Report the malaria status of this cell.
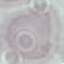

Uninfected.

capture = smartphone through the microscope eyepiece
preparation = thin smear
stain = Giemsa
image type = automatically extracted cell patch, resized to 64 × 64 pixels